Report the malaria status of this cell.
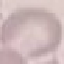
Uninfected.

stain = Giemsa
image type = automatically extracted cell patch, resized to 64 × 64 pixels
preparation = thin blood film
capture = smartphone camera at the microscope eyepiece